Identify the parasite.
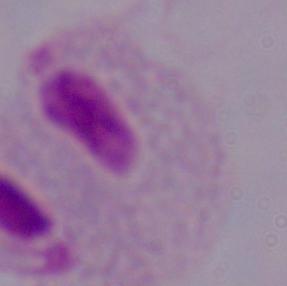
A trichomonad.

{
  "magnification": "1000x",
  "modality": "micrograph"
}